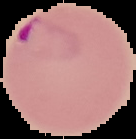

{
  "result": "Plasmodium parasites detected",
  "preparation": "thin blood film",
  "image_type": "segmented cell region on a black background",
  "image_size": "136×139 pixels"
}